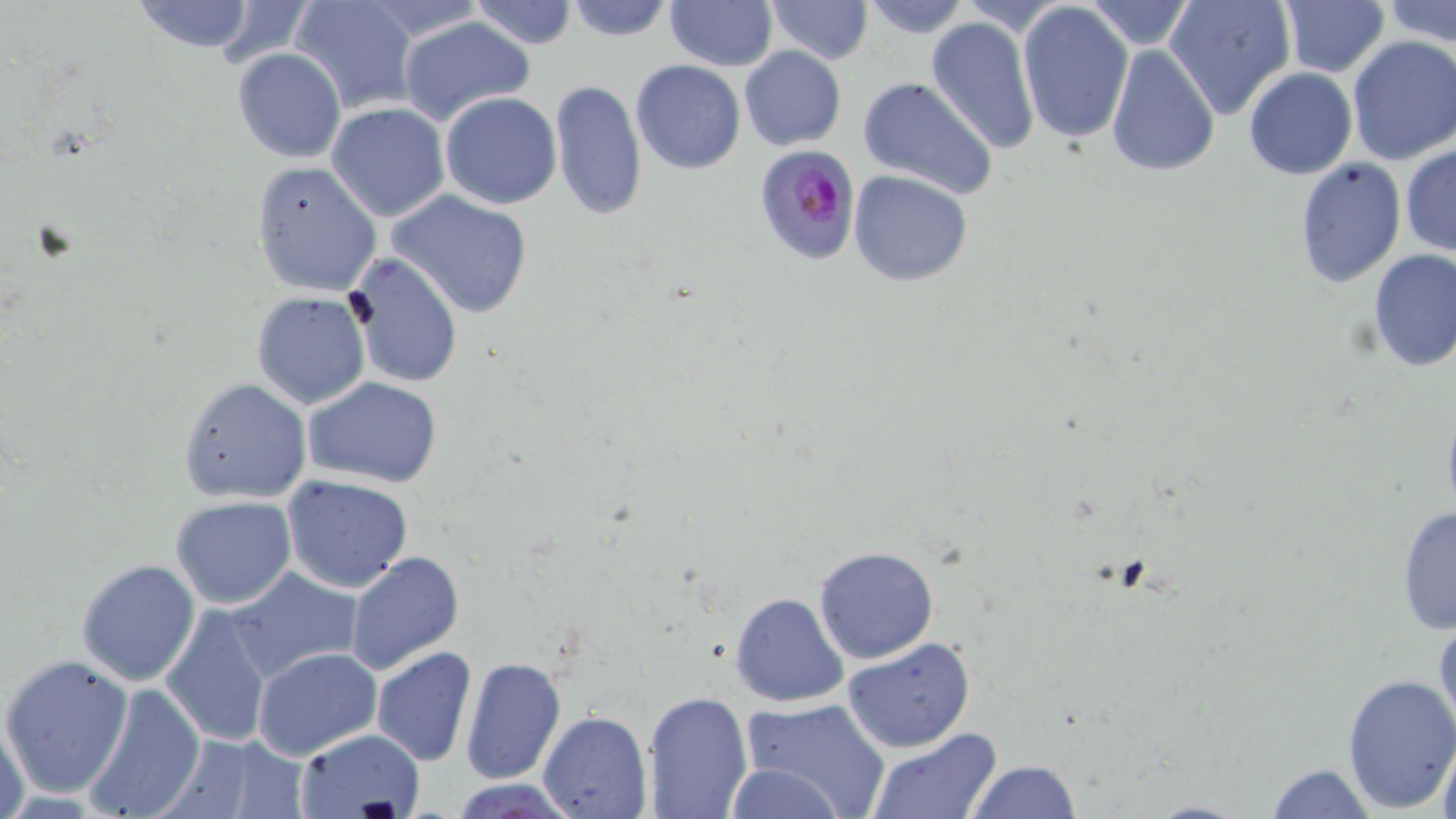

Approximate bounding boxes as (x1, y1, x2, y2) in pixels. Plasmodium falciparum-infected red blood cell locations: (754, 143, 859, 266). Uninfected red blood cell locations: (130, 0, 260, 54), (289, 0, 418, 114), (470, 0, 579, 50), (563, 0, 677, 42), (757, 0, 864, 131), (763, 0, 872, 64), (858, 0, 973, 38), (956, 0, 1074, 35), (1084, 0, 1197, 52), (1164, 0, 1296, 119), (1278, 0, 1390, 78), (1385, 0, 1456, 47), (358, 1, 489, 47), (665, 1, 776, 71), (1018, 1, 1135, 144), (212, 2, 313, 68), (397, 15, 536, 127), (925, 16, 1040, 155), (1346, 37, 1456, 166), (1104, 42, 1219, 178), (738, 45, 846, 151), (232, 46, 345, 163), (631, 59, 744, 174), (1244, 67, 1358, 181), (858, 76, 1000, 200), (549, 78, 647, 221), (440, 92, 562, 209), (326, 102, 449, 221), (1401, 145, 1456, 258), (1294, 155, 1406, 288), (250, 161, 382, 297), (847, 169, 974, 287), (387, 190, 534, 319), (1366, 249, 1456, 372), (347, 252, 463, 389), (250, 291, 373, 410), (304, 376, 445, 490), (177, 377, 311, 503), (281, 474, 414, 593), (170, 497, 298, 609), (1395, 503, 1455, 635), (813, 545, 939, 665), (345, 552, 465, 678), (75, 558, 200, 686), (228, 567, 361, 683), (731, 592, 850, 707), (160, 604, 276, 748), (1433, 608, 1455, 740), (841, 637, 974, 753), (253, 647, 382, 762), (371, 647, 477, 766), (1, 653, 133, 800), (460, 655, 567, 785), (1340, 672, 1455, 815), (79, 684, 208, 819), (641, 690, 753, 818), (739, 698, 893, 817), (538, 710, 651, 818), (1, 712, 31, 819), (293, 728, 426, 819), (1435, 730, 1456, 819), (867, 731, 1001, 818), (158, 733, 307, 818), (965, 759, 1083, 817), (725, 761, 847, 818), (1263, 762, 1378, 818), (453, 778, 577, 817), (1133, 800, 1257, 819). Slide-level diagnosis: Plasmodium falciparum. Optical microscopy. May-Grünwald-Giemsa-stained preparation. 1000x magnification. Single field of view. Thin blood smear. Image is 1456×819 pixels.